Identify the preparation type.
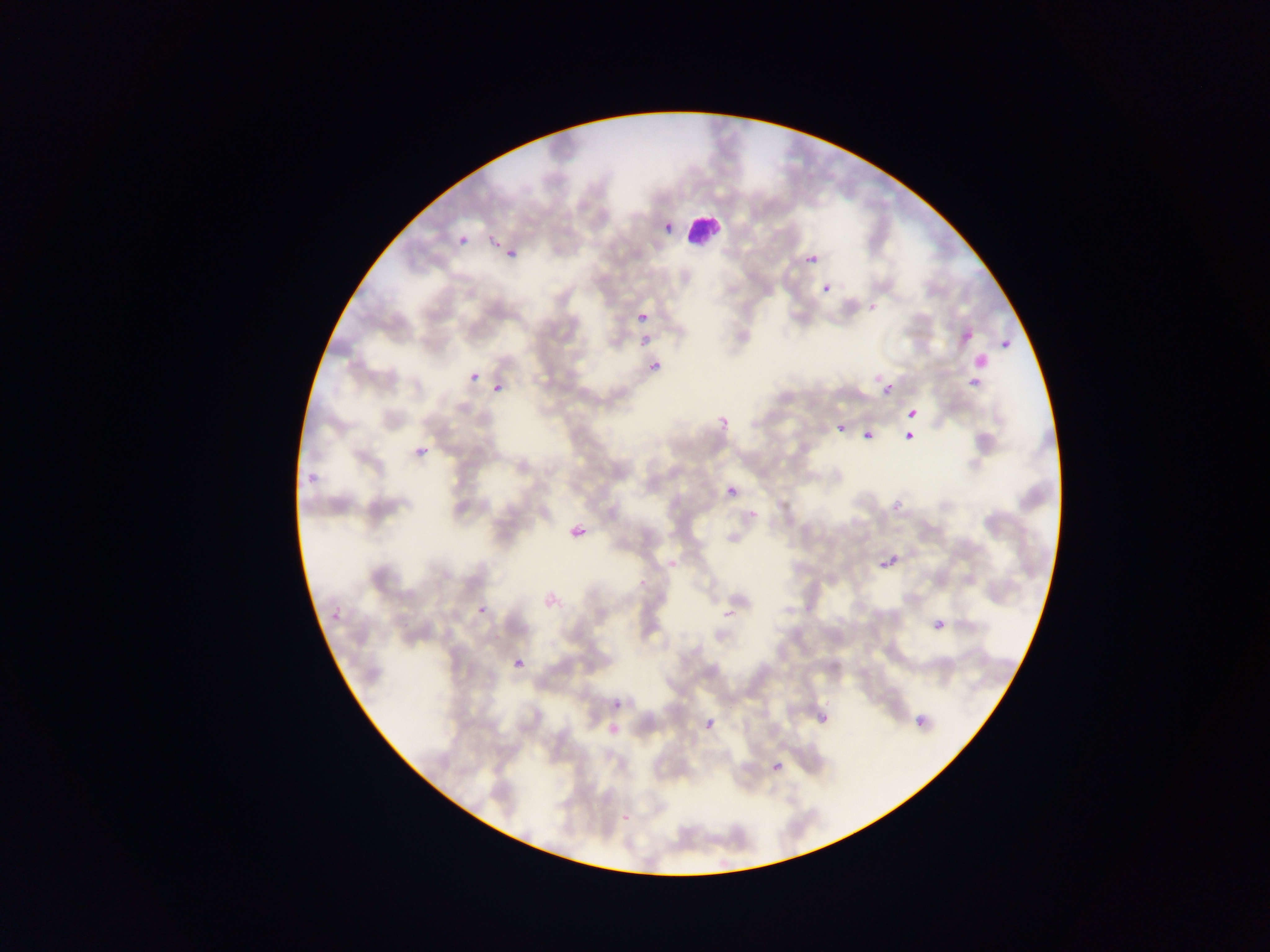
This is a thin smear.

Approximate bounding boxes as (left, top, right, bottom) in pixels. Plasmodium parasite locations: (450, 223, 475, 251), (494, 240, 522, 268), (806, 254, 818, 265), (822, 284, 832, 294), (622, 314, 643, 331), (954, 321, 971, 341), (638, 340, 678, 366), (1001, 340, 1010, 349), (959, 347, 987, 373), (465, 362, 472, 383), (962, 369, 983, 404), (486, 370, 507, 396), (875, 375, 893, 396), (708, 393, 741, 429), (900, 395, 920, 428), (896, 421, 913, 446), (837, 423, 845, 432), (864, 430, 876, 439), (414, 444, 429, 458), (301, 450, 324, 483), (714, 476, 731, 499), (564, 507, 585, 548), (870, 531, 905, 574), (321, 583, 354, 628), (470, 605, 480, 618), (933, 618, 947, 631), (511, 658, 524, 670), (612, 699, 623, 709), (705, 718, 715, 728), (916, 718, 925, 727), (772, 761, 784, 772), (623, 814, 631, 822). Leukocyte locations: (683, 209, 721, 246). Collected in Ghana. Image is 1270×952 pixels. Mobile-phone photograph taken through the microscope. One field of view.